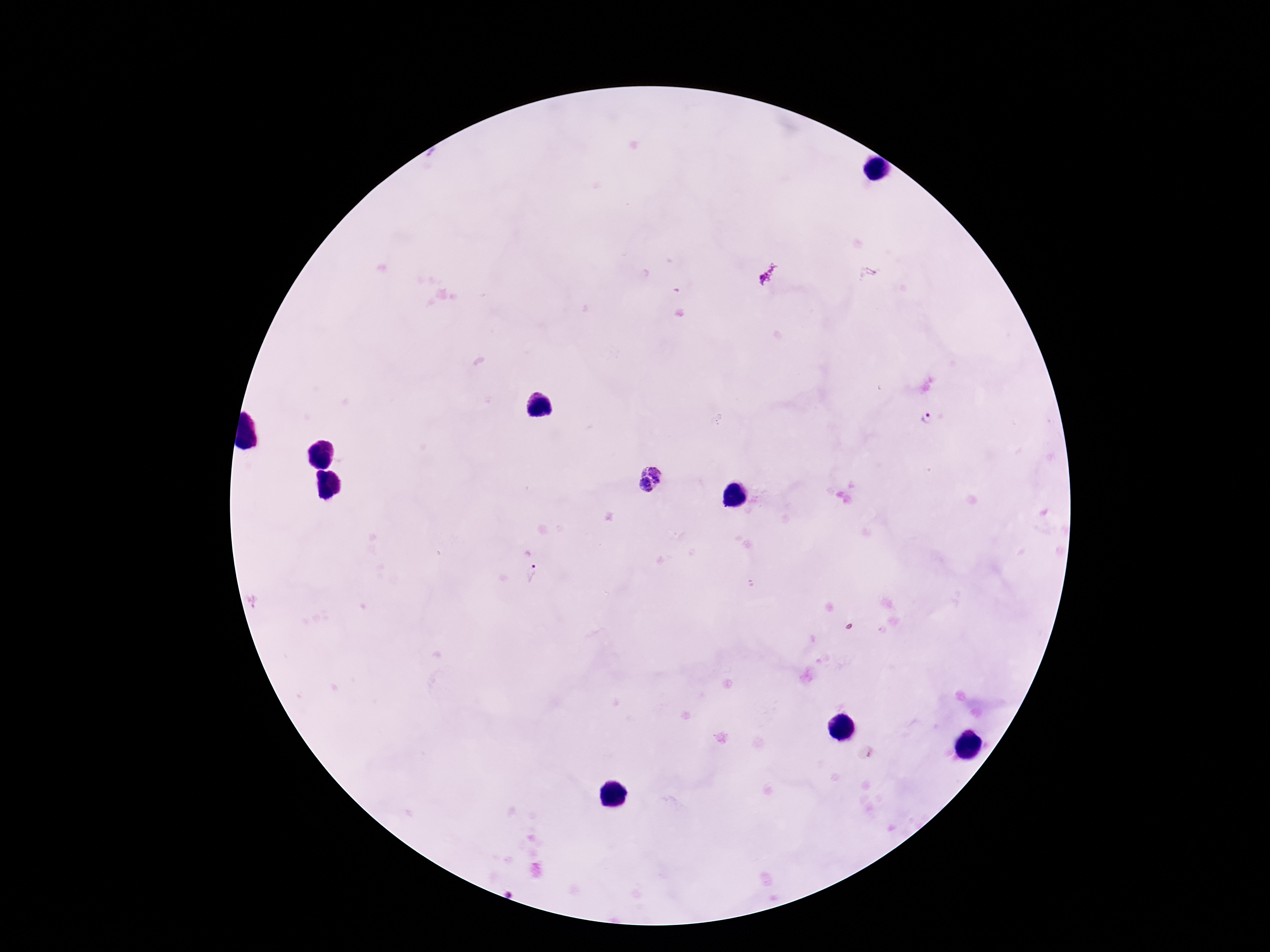 Approximate centers as {x, y} in pixels. Plasmodium parasite locations: {928, 419}, {650, 480}, {532, 570}. Single field of view. Giemsa stain. Image is 1270×952 pixels. 100x magnification. Patient malaria status: infected. Photographed through the microscope eyepiece with a smartphone camera. Thick peripheral-blood smear.